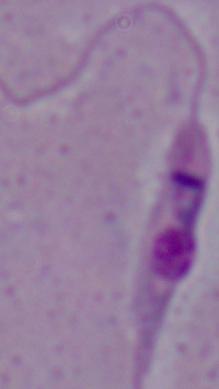

Summary:
  - Identification: Leishmania
  - Modality: photomicrograph
  - Magnification: 1000x